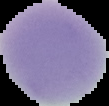
Image is 109×106 pixels. Result: no malaria parasites seen. The area outside the segmented cell region is set to black. From a thin blood smear.